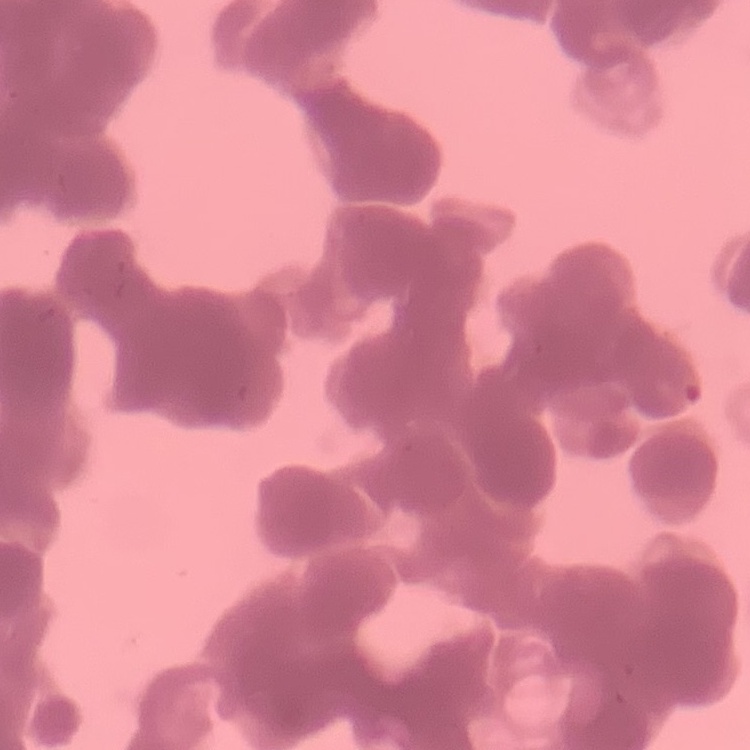
Summary:
  - Red blood cell morphology: rouleaux formation
  - Image type: square crop of a larger photomicrograph
  - Stain: Field's or Giemsa
  - Preparation: thin blood film